Assess the morphology of the red blood cells.
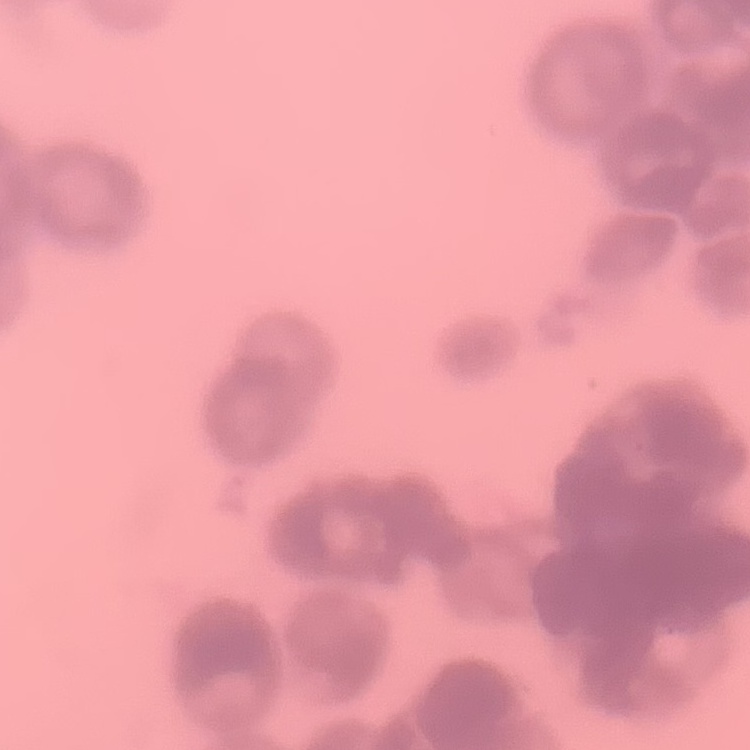

They show rouleaux formation.

One tile cut from a larger photomicrograph. Thin blood smear. Stained with either Field's or Giemsa.